Classify this cell by malaria status.
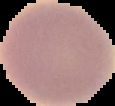

It is uninfected.

Summary:
  - Image size: 115×106 pixels
  - Preparation: thin blood smear
  - Image type: segmented cell region on a black background